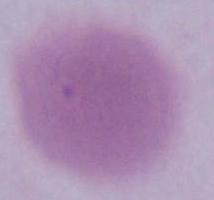

{
  "modality": "micrograph",
  "identification": "erythrocyte",
  "magnification": "1000x"
}